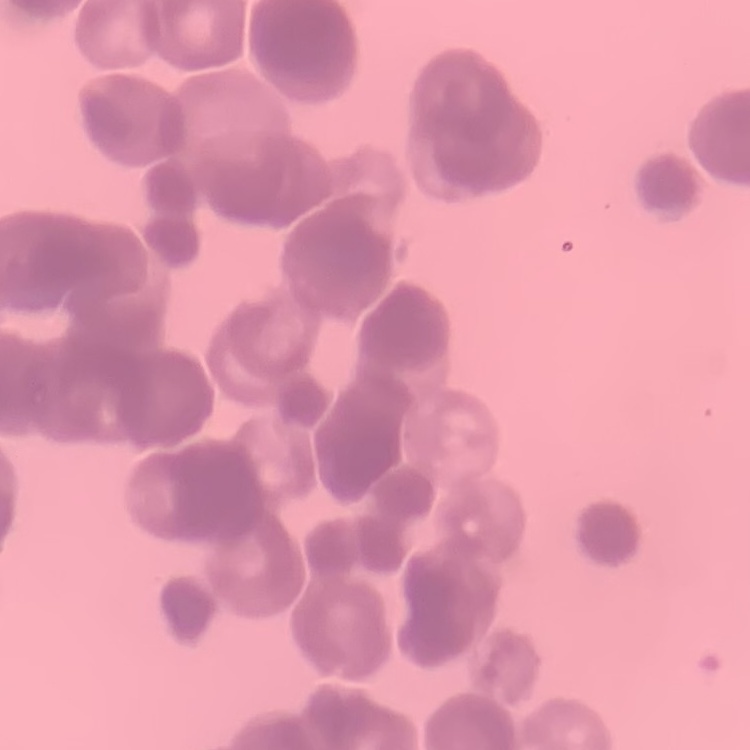
The red blood cells show rouleaux formation. Thin blood smear. One tile cut from a larger photomicrograph. Stained with either Field's or Giemsa.